Describe the morphology of the erythrocytes.
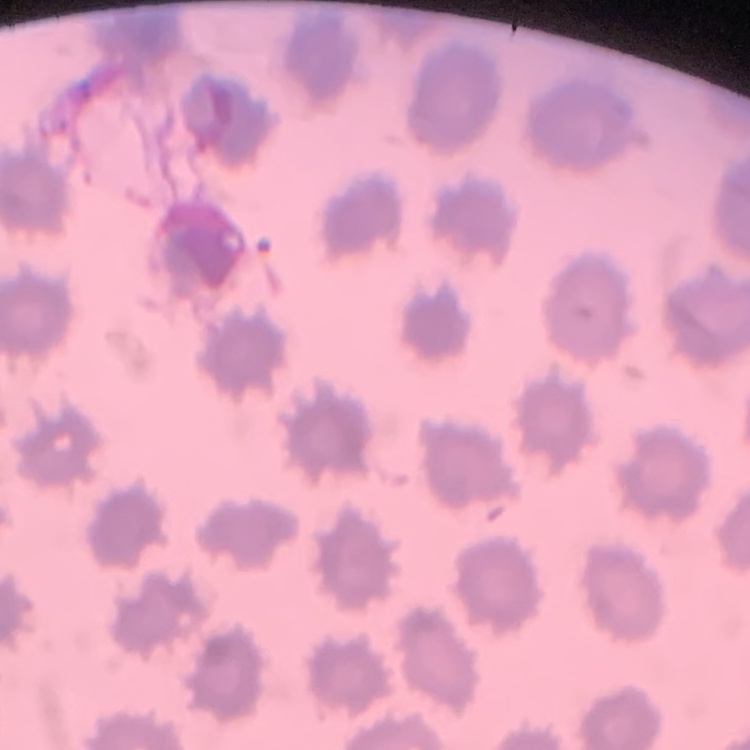

They show no rouleaux formation.

Thin peripheral smear. Stained with either Field's or Giemsa. One tile cut from a larger photomicrograph.